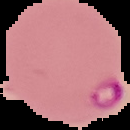
Summary:
  - Malaria status: parasitized
  - Image size: 130×130 pixels
  - Image type: segmented cell region on a black background
  - Preparation: thin blood film